Assess the morphology of the erythrocytes.
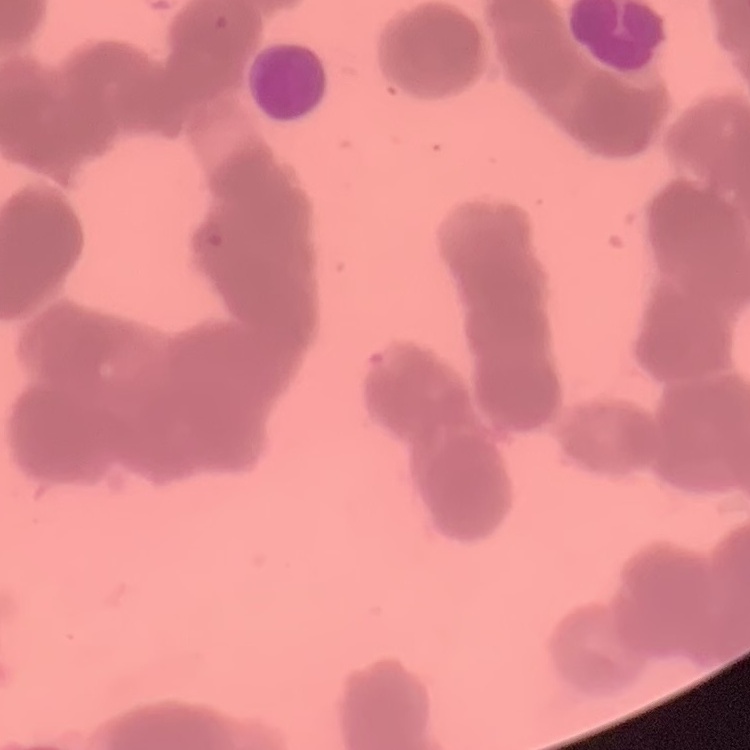

Rouleaux formation.

Summary:
  - Image type: square crop of a larger photomicrograph
  - Preparation: thin blood film
  - Stain: Field's or Giemsa